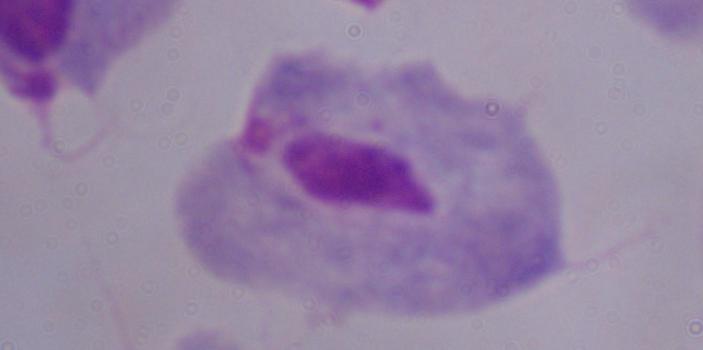
{
  "modality": "micrograph",
  "identification": "trichomonad",
  "magnification": "1000x"
}